Assess this cell for malaria.
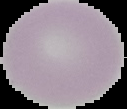

Uninfected.

Summary:
  - Preparation: thin blood film
  - Image size: 127×109 pixels
  - Image type: cell region segmented out of the field of view; surrounding area masked to black